Give the extent of all Plasmodium vivax-infected red blood cells.
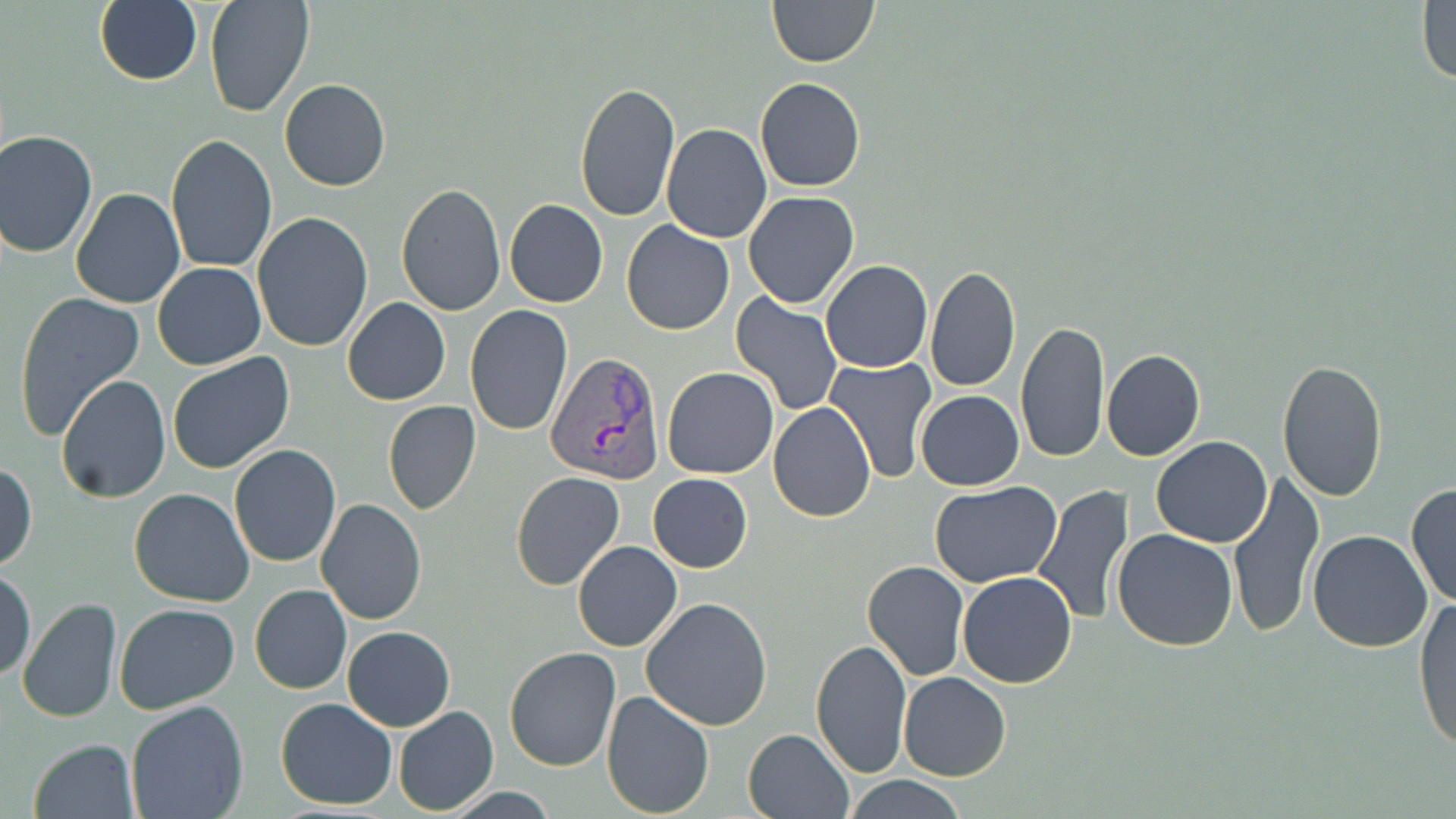

Approximate bounding boxes as (x1, y1, x2, y2) in pixels.
Plasmodium vivax-infected red blood cells: (546, 351, 665, 484).

Uninfected red blood cell locations: (95, 0, 203, 86), (203, 0, 314, 119), (767, 0, 879, 67), (1417, 2, 1456, 88), (754, 76, 865, 192), (278, 79, 390, 191), (575, 81, 680, 220), (661, 122, 771, 243), (0, 130, 98, 257), (167, 134, 277, 275), (394, 184, 506, 316), (70, 187, 185, 309), (743, 191, 859, 309), (504, 200, 608, 308), (252, 213, 374, 352), (622, 220, 734, 336), (821, 259, 932, 372), (151, 262, 267, 369), (925, 265, 1021, 394), (12, 291, 145, 441), (730, 293, 844, 418), (343, 297, 450, 406), (465, 305, 572, 435), (1016, 320, 1110, 464), (1102, 349, 1205, 462), (166, 352, 294, 475), (825, 357, 935, 484), (1276, 361, 1390, 502), (663, 367, 779, 479), (57, 375, 171, 504), (915, 390, 1024, 491), (383, 400, 481, 514), (768, 402, 876, 523), (1150, 437, 1272, 548), (229, 445, 342, 567), (0, 461, 37, 571), (512, 472, 625, 590), (648, 473, 752, 573), (1228, 475, 1323, 639), (930, 481, 1063, 586), (1407, 483, 1456, 611), (1031, 485, 1134, 627), (128, 487, 254, 607), (316, 498, 426, 624), (1112, 527, 1238, 650), (1308, 530, 1433, 652), (572, 541, 683, 651), (862, 560, 969, 680), (1, 565, 36, 680), (955, 571, 1078, 688), (250, 584, 351, 696), (1413, 595, 1456, 749), (639, 597, 773, 731), (17, 598, 122, 723), (113, 604, 239, 714), (342, 626, 454, 730), (810, 638, 913, 779), (504, 647, 621, 772), (898, 671, 1012, 782), (600, 690, 715, 818), (124, 698, 250, 819), (274, 698, 398, 809), (393, 706, 498, 814), (743, 729, 853, 818), (28, 738, 140, 819), (842, 776, 969, 817). Slide-level diagnosis: Plasmodium vivax. Thin blood film. Image is 1456×819 pixels. One field of a larger specimen. 1000x magnification. May-Grünwald-Giemsa stain. Optical microscopy.